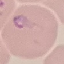

result = malaria parasites detected
preparation = thin blood film
capture = smartphone camera at the microscope eyepiece
stain = Giemsa
image type = automatically extracted cell patch, resized to 64 × 64 pixels